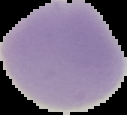

image_size: 127×115 pixels
preparation: thin blood film
malaria_status: uninfected
image_type: segmented cell region with the area outside set to black